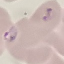
Summary:
  - Malaria status: parasitized
  - Image type: automatically extracted cell patch, resized to 64 × 64 pixels
  - Preparation: thin blood film
  - Capture: smartphone through the microscope eyepiece
  - Stain: Giemsa